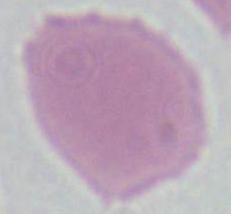 Photomicrograph. 1000x magnification. An erythrocyte is seen.